Describe the morphology of the erythrocytes.
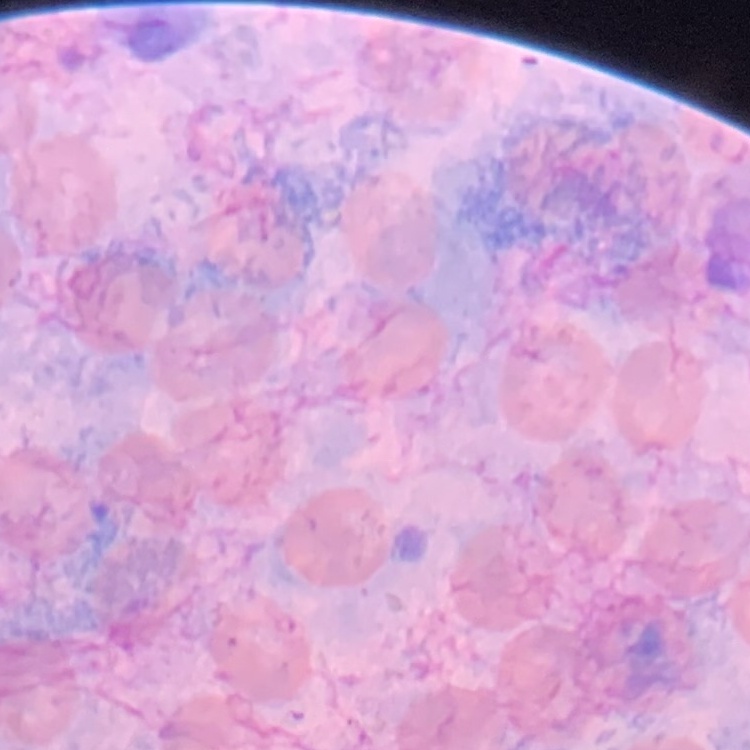
They show no rouleaux formation.

{
  "stain": "Field's or Giemsa",
  "preparation": "thin peripheral smear",
  "image_type": "one tile cut from a larger photomicrograph"
}